Assess this cell for malaria.
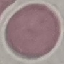
It is uninfected.

Cell patch, automatically extracted from a larger field of view and resized to 64 × 64 pixels. Giemsa-stained preparation. Thin blood smear. Photographed with a smartphone camera at the microscope eyepiece.